Identify the parasite.
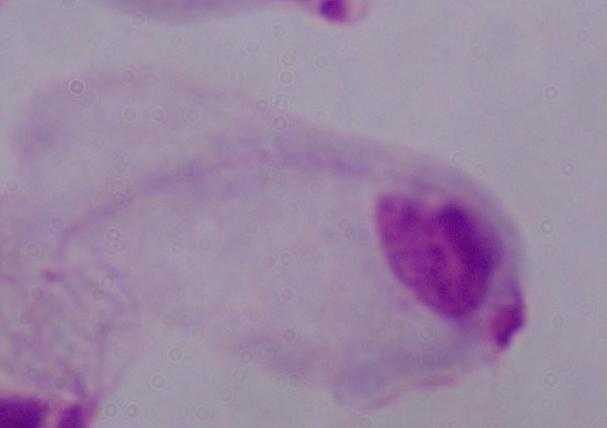

This is a trichomonad.

magnification = 1000x
modality = photomicrograph